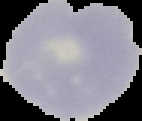

image size = 142×121 pixels
image type = segmented cell region on a black background
malaria status = uninfected
preparation = thin blood smear